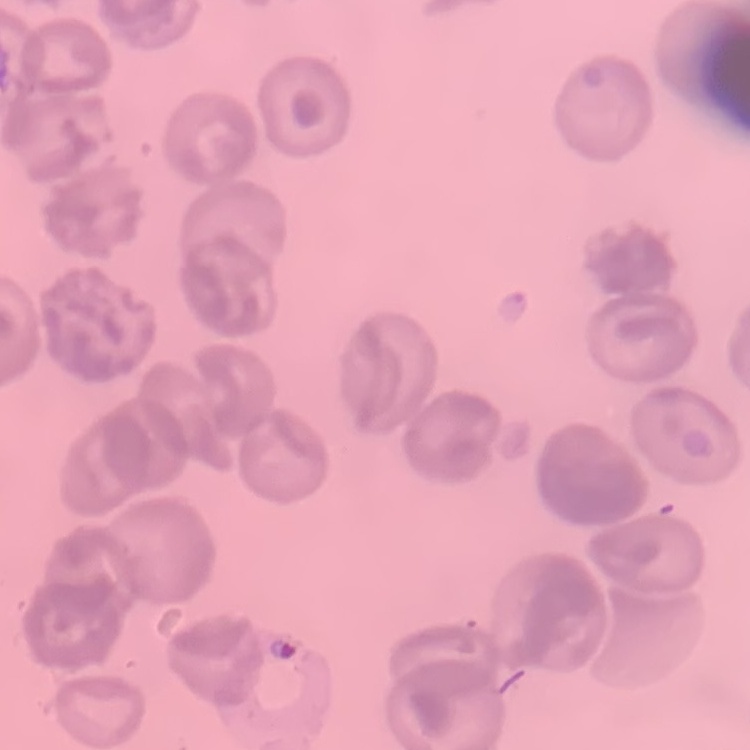 The red blood cells show no rouleaux formation. Thin blood film. One tile cut from a larger photomicrograph. Stained with either Field's or Giemsa.